Identify the parasite.
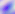

Toxoplasma gondii.

modality = photomicrograph
magnification = 400x